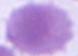

Summary:
  - Magnification: 1000x
  - Modality: photomicrograph
  - Identification: red blood cell